Report the malaria status of this cell.
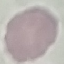

It is uninfected.

Summary:
  - Preparation: thin blood film
  - Stain: Giemsa
  - Image type: cell patch, automatically extracted from a larger field of view and resized to 64 × 64 pixels
  - Capture: smartphone through the microscope eyepiece